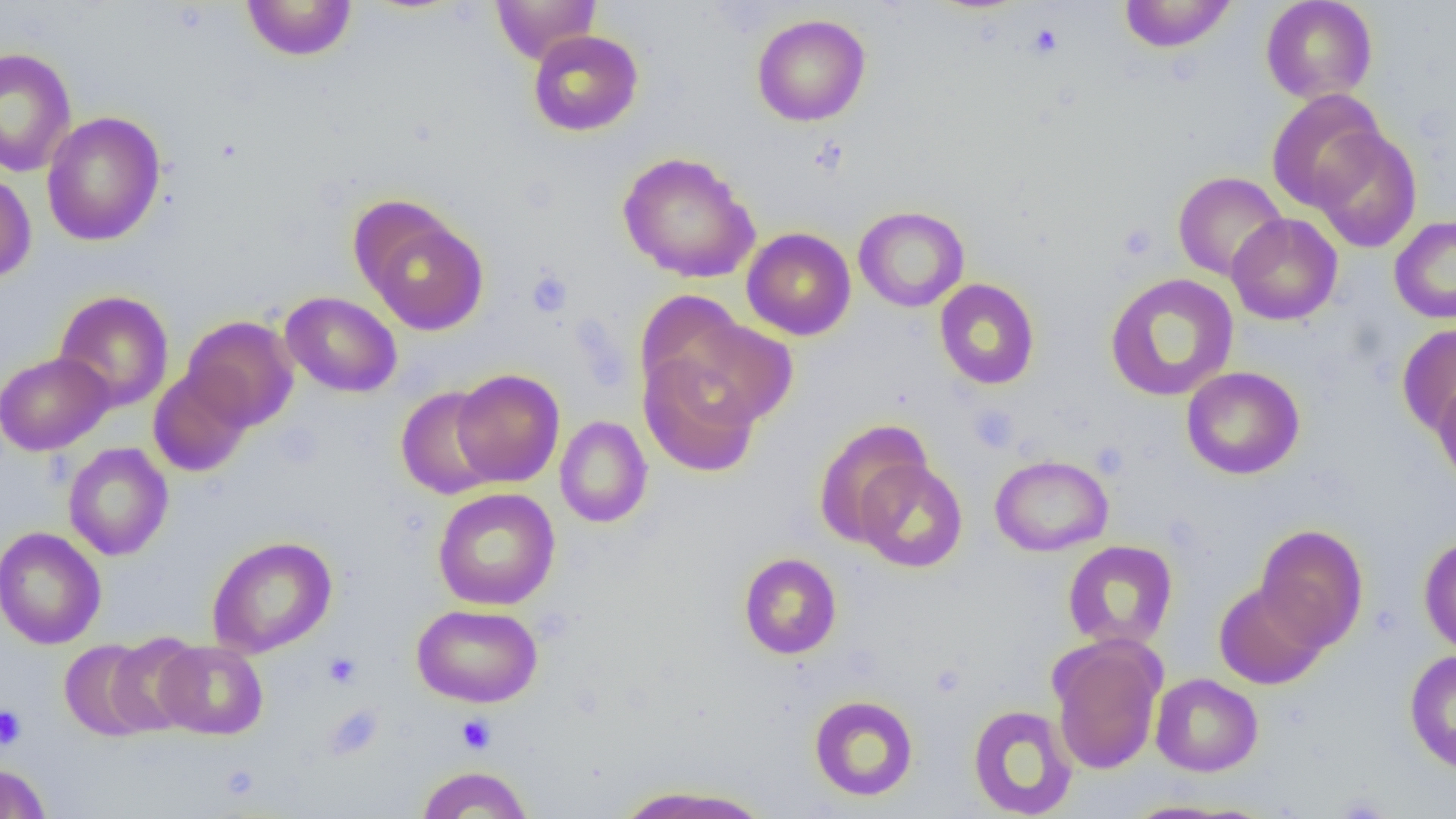
Approximate bounding boxes as (x1,y1)-(x2,y2) corner pairs in pixels. Platelet locations: (1027,24)-(1063,58), (1117,222)-(1158,262), (526,270)-(572,317), (968,404)-(1019,453), (323,652)-(362,688), (0,704)-(27,750), (456,714)-(496,754). Uninfected red blood cell locations: (490,0)-(601,64), (1118,0)-(1238,53), (1260,0)-(1378,104), (241,1)-(357,61), (751,14)-(871,127), (528,30)-(643,137), (0,47)-(76,177), (1266,89)-(1387,212), (41,111)-(166,246), (1310,127)-(1423,254), (617,152)-(761,283), (0,171)-(37,283), (1172,171)-(1288,282), (357,205)-(489,335), (854,206)-(969,312), (1227,213)-(1343,326), (1389,215)-(1456,324), (742,227)-(856,340), (1104,273)-(1239,402), (934,278)-(1040,390), (53,290)-(174,412), (280,291)-(402,397), (635,292)-(758,413), (665,314)-(799,428), (182,315)-(298,430), (1397,323)-(1456,436), (0,351)-(113,456), (638,352)-(761,478), (1181,366)-(1305,480), (148,368)-(254,477), (451,369)-(565,487), (1432,377)-(1456,490), (395,386)-(503,500), (555,415)-(652,528), (813,420)-(931,546), (62,442)-(174,560), (989,454)-(1113,556), (854,459)-(968,572), (432,487)-(561,610), (1255,523)-(1368,652), (0,526)-(106,650), (1419,534)-(1456,657), (207,535)-(337,658), (1062,540)-(1178,650), (738,552)-(842,659), (1214,580)-(1328,689), (412,603)-(543,708), (105,632)-(204,736), (1049,635)-(1166,775), (59,639)-(160,741), (155,640)-(268,740), (1404,649)-(1456,773), (1150,673)-(1263,776), (809,695)-(919,801), (967,704)-(1078,818), (0,763)-(52,819), (415,765)-(533,818), (612,784)-(773,819), (1116,799)-(1255,818). Slide-level diagnosis: negative for blood parasites. Optical microscopy. 1000x magnification. Image is 1456×819 pixels. Thin blood film. Single field of view.